Assess the morphology of the red blood cells.
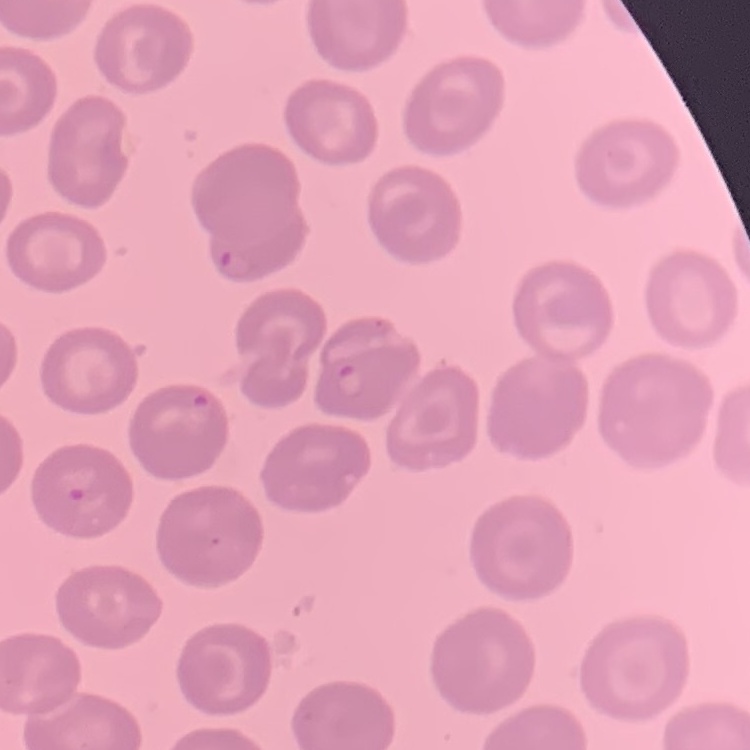

No rouleaux formation.

One tile cut from a larger photomicrograph. Field's or Giemsa stain. Thin blood smear.